Name the parasite shown.
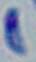

Toxoplasma gondii.

magnification = 1000x
modality = photomicrograph